Assess this cell for malaria.
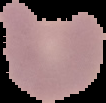
Parasitized.

From a thin blood smear. Image is 106×103 pixels. Segmented cell region on a black background.